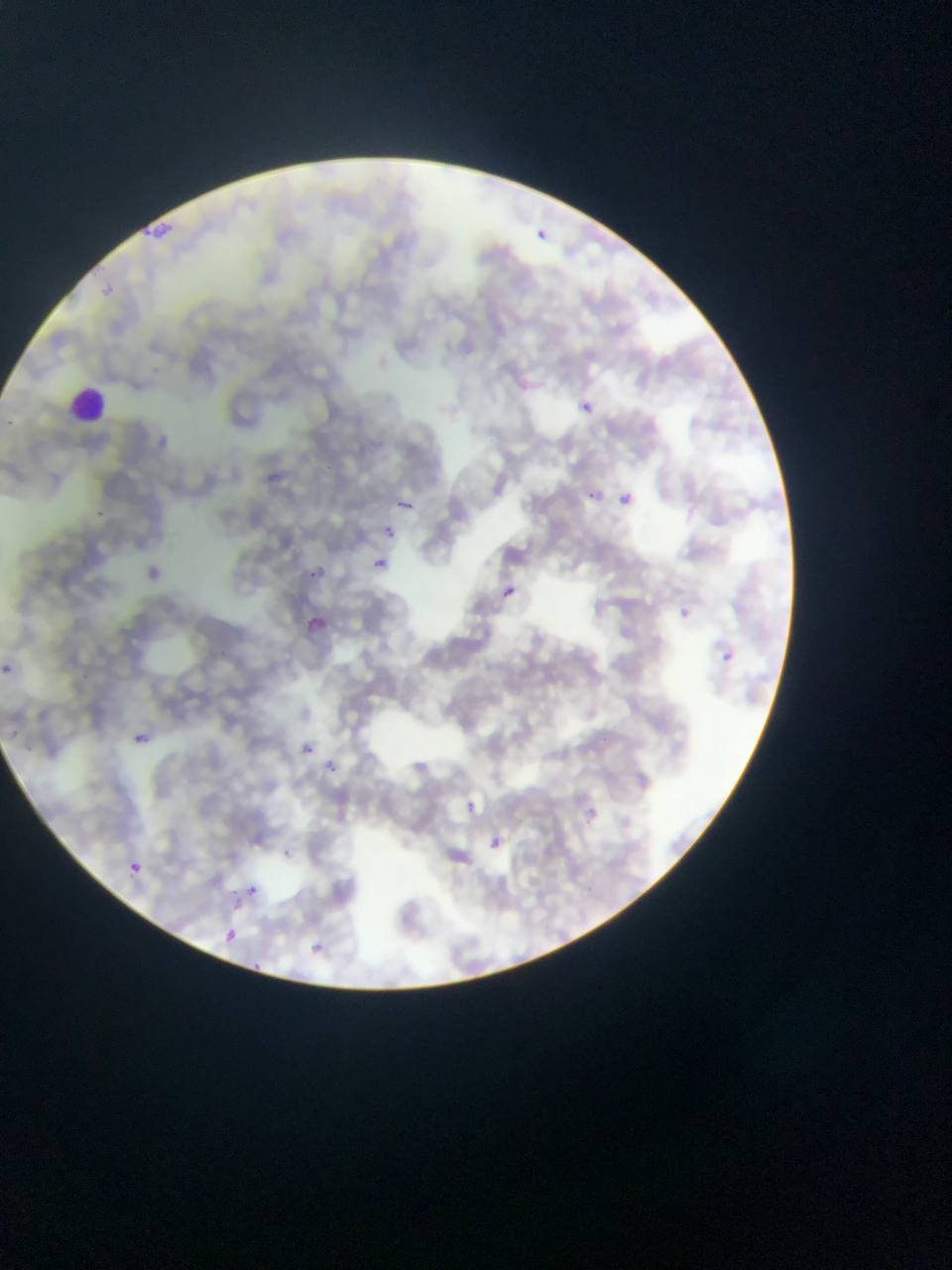
plasmodium_parasite_locations: 'approximate bounding boxes as (left, top, right, bottom) in pixels: (139, 225, 161, 248), (162, 225, 172, 232), (535, 228, 550, 241), (515, 376, 533, 394), (578, 398, 596, 414), (156, 432, 175, 450), (257, 462, 290, 494), (586, 489, 599, 500), (620, 493, 633, 506), (393, 497, 417, 521), (372, 516, 401, 540), (363, 556, 386, 575), (143, 558, 176, 595), (312, 563, 332, 583), (503, 586, 516, 599), (680, 608, 692, 620), (310, 610, 342, 635), (720, 651, 733, 663), (3, 663, 15, 674), (134, 733, 151, 744), (301, 735, 332, 760), (326, 749, 349, 783), (467, 797, 482, 812), (585, 807, 600, 824), (482, 834, 514, 870), (130, 861, 144, 874), (240, 879, 274, 896), (223, 925, 241, 943), (308, 936, 327, 951)'
capture: mobile-phone photograph through a microscope
image_size: 952×1270 pixels
country: Ghana
leukocyte_locations: 'approximate bounding boxes as (left, top, right, bottom) in pixels: (68, 386, 108, 421)'
preparation: thin blood smear
field_of_view: single